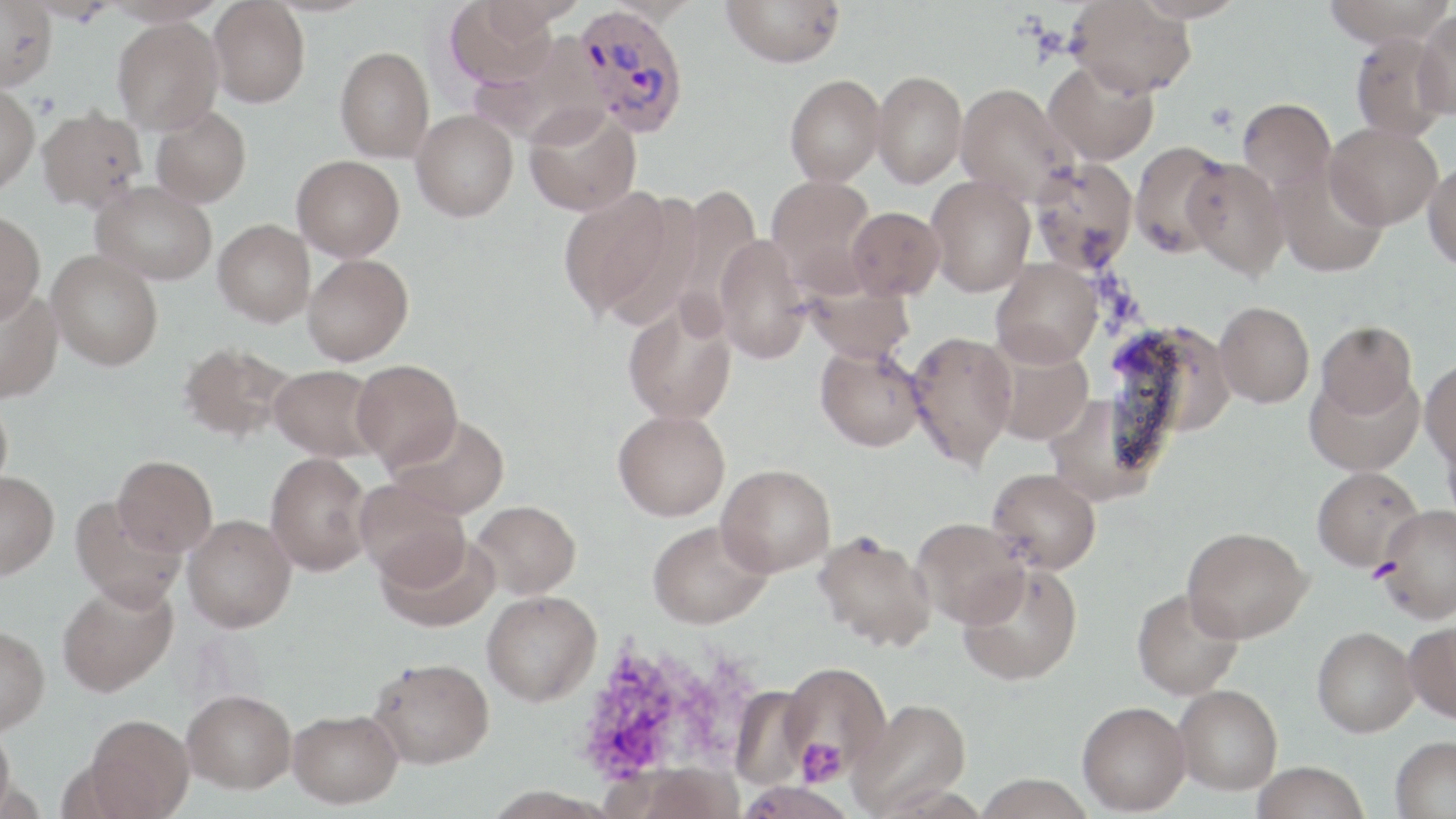

Summary:
  - Coordinate format: approximate bounding boxes as [x1, y1, x2, y2] in pixels
  - Platelet locations: [29, 92, 60, 119], [591, 653, 678, 771], [796, 738, 847, 785]
  - Uninfected red blood cell locations: [23, 0, 118, 25], [101, 0, 228, 26], [445, 0, 558, 90], [721, 0, 846, 67], [1130, 0, 1247, 23], [1321, 0, 1455, 47], [0, 1, 56, 90], [208, 1, 310, 108], [1067, 1, 1196, 97], [1415, 9, 1456, 122], [113, 17, 223, 134], [1350, 32, 1452, 141], [336, 46, 435, 163], [1044, 60, 1159, 165], [872, 69, 967, 188], [784, 74, 886, 186], [955, 81, 1074, 202], [0, 84, 40, 193], [1237, 97, 1335, 194], [524, 105, 641, 216], [151, 106, 251, 208], [37, 107, 146, 212], [411, 109, 518, 221], [1324, 122, 1443, 230], [1127, 140, 1232, 259], [292, 155, 404, 261], [1183, 157, 1289, 280], [1029, 158, 1139, 274], [1271, 161, 1390, 278], [1423, 161, 1456, 272], [766, 175, 878, 291], [925, 175, 1036, 296], [92, 181, 217, 285], [558, 184, 679, 322], [661, 184, 761, 330], [847, 206, 944, 300], [0, 210, 45, 322], [213, 219, 315, 326], [714, 233, 811, 364], [47, 249, 163, 370], [303, 254, 414, 365], [991, 258, 1103, 368], [801, 275, 915, 364], [0, 287, 62, 403], [622, 297, 738, 425], [1214, 301, 1315, 408], [1104, 320, 1232, 459], [1315, 320, 1417, 419], [907, 330, 1017, 470], [179, 342, 296, 442], [815, 345, 926, 451], [991, 346, 1094, 444], [1420, 357, 1456, 471], [352, 359, 462, 469], [270, 364, 383, 462], [1305, 370, 1423, 476], [0, 394, 12, 498], [613, 409, 730, 521], [388, 414, 510, 519], [266, 452, 373, 576], [113, 455, 217, 556], [716, 464, 836, 577], [1312, 466, 1424, 572], [987, 467, 1101, 574], [0, 471, 59, 580], [358, 479, 471, 589], [71, 495, 186, 611], [471, 500, 581, 599], [1377, 506, 1456, 622], [183, 514, 296, 632], [912, 517, 1029, 628], [648, 520, 772, 629], [1182, 526, 1311, 642], [812, 531, 936, 652], [376, 532, 500, 632], [956, 562, 1083, 686], [56, 580, 178, 697], [1132, 588, 1245, 699], [482, 590, 601, 706], [1404, 620, 1456, 723], [0, 625, 50, 734], [1312, 626, 1419, 737], [369, 657, 494, 768], [781, 662, 891, 777], [1174, 684, 1282, 795], [729, 686, 815, 789], [183, 688, 297, 793], [849, 698, 972, 816], [1078, 701, 1191, 815], [288, 708, 403, 808], [85, 714, 194, 817], [0, 726, 17, 818], [1390, 735, 1456, 819], [1250, 761, 1370, 819], [624, 762, 745, 819], [975, 774, 1095, 819], [734, 780, 856, 819]
  - Plasmodium vivax-infected red blood cell locations: [574, 5, 689, 137]
  - Slide-level diagnosis: Plasmodium vivax
  - Modality: light microscopy
  - Field of view: one of a larger specimen
  - Magnification: 1000x
  - Stain: May-Grünwald-Giemsa
  - Preparation: thin blood smear
  - Image size: 1456×819 pixels